Name the cell type shown.
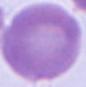
An erythrocyte.

Summary:
  - Magnification: 1000x
  - Modality: micrograph